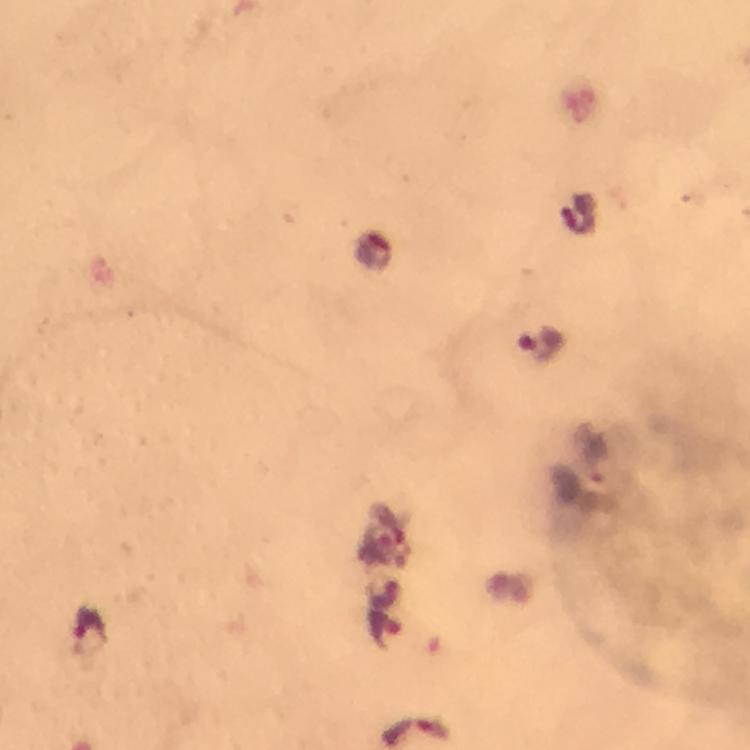
Approximate object centers, in pixels from the top-left corner. Plasmodium parasite locations: (x=580, y=213), (x=374, y=253), (x=538, y=341), (x=384, y=596), (x=90, y=629), (x=383, y=630), (x=417, y=732). Thick blood smear. From a diagnostic examination for malaria. Image is 750×750 pixels. At 100x magnification. Immersion oil applied. A crop from one field of view. Photographed with a smartphone mounted on the microscope. Giemsa-stained preparation.